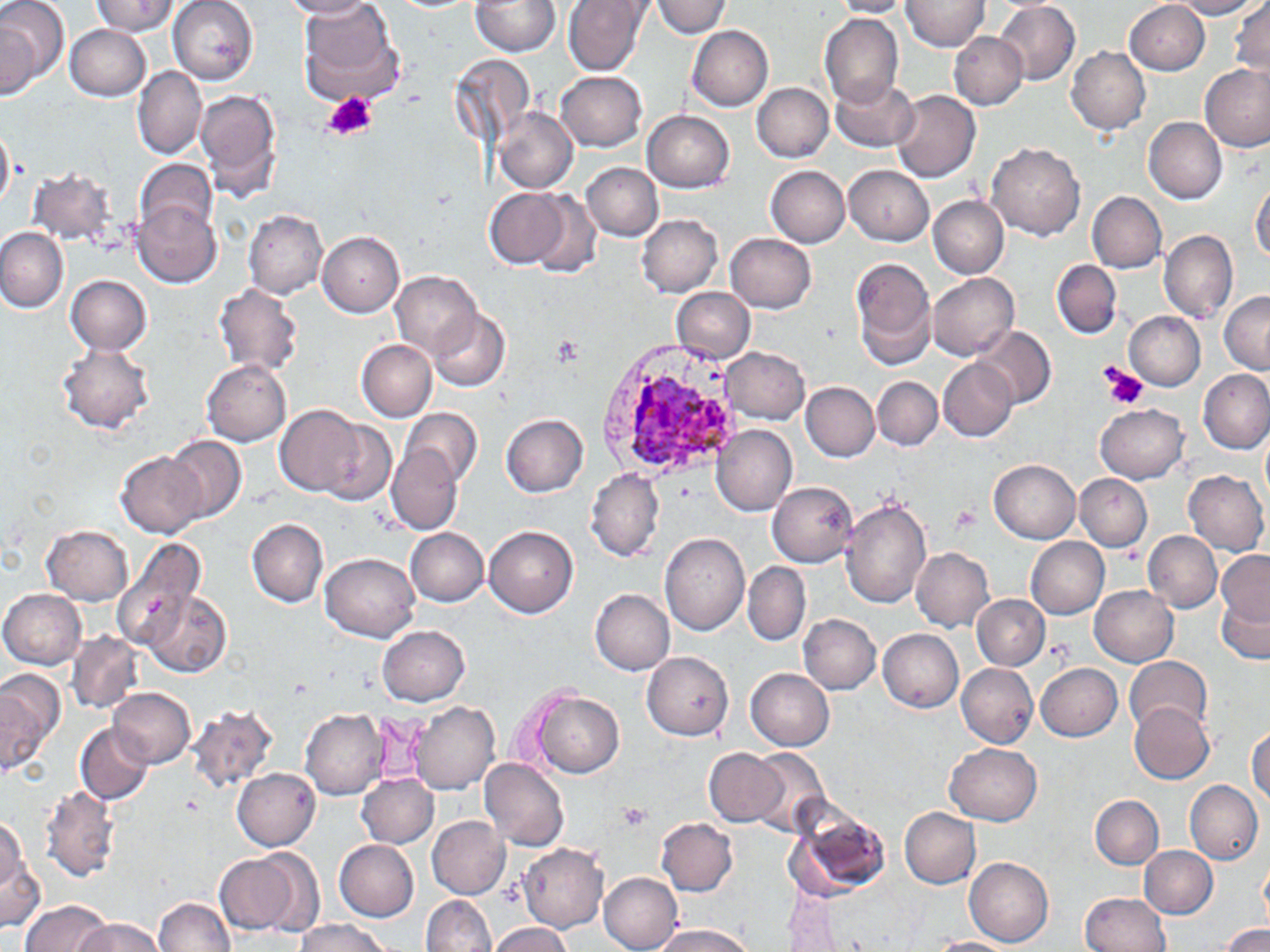
Approximate bounding boxes as (x1, y1, x2, y2) in pixels. Plasmodium vivax-infected red blood cell locations: (594, 337, 750, 482). Uninfected red blood cell locations: (0, 0, 67, 96), (169, 0, 258, 84), (282, 0, 378, 17), (471, 0, 560, 55), (562, 0, 650, 76), (651, 0, 733, 38), (1169, 0, 1266, 19), (91, 1, 180, 36), (299, 1, 408, 108), (832, 1, 912, 18), (901, 1, 991, 51), (1125, 1, 1210, 75), (996, 2, 1080, 85), (1231, 2, 1270, 79), (819, 13, 904, 106), (3, 16, 40, 100), (65, 25, 149, 100), (687, 26, 773, 111), (949, 32, 1026, 110), (1065, 48, 1150, 133), (1200, 64, 1269, 151), (132, 66, 206, 159), (558, 71, 646, 151), (830, 75, 918, 152), (752, 83, 833, 161), (196, 88, 282, 201), (889, 89, 979, 184), (495, 108, 576, 193), (643, 110, 735, 192), (1143, 116, 1226, 204), (0, 124, 15, 212), (986, 143, 1086, 241), (138, 159, 214, 237), (583, 162, 663, 241), (765, 166, 849, 247), (845, 166, 934, 246), (28, 167, 115, 248), (1250, 181, 1270, 264), (485, 188, 570, 266), (1087, 191, 1166, 272), (529, 192, 600, 277), (928, 197, 1008, 278), (134, 202, 221, 286), (243, 207, 327, 297), (637, 214, 722, 296), (0, 226, 69, 313), (1159, 230, 1237, 322), (318, 231, 404, 316), (726, 234, 816, 312), (851, 256, 938, 368), (1051, 259, 1121, 339), (393, 272, 481, 360), (927, 272, 1020, 360), (66, 275, 150, 354), (214, 283, 304, 377), (671, 287, 754, 363), (1218, 289, 1270, 373), (427, 309, 512, 391), (1125, 311, 1205, 390), (972, 327, 1055, 409), (357, 340, 436, 420), (58, 344, 154, 433), (721, 347, 810, 423), (939, 359, 1016, 441), (202, 360, 292, 446), (1199, 368, 1270, 453), (873, 376, 941, 449), (801, 382, 879, 461), (1094, 403, 1189, 483), (275, 406, 367, 496), (400, 408, 482, 489), (501, 413, 590, 496), (319, 417, 396, 506), (712, 426, 797, 515), (1260, 426, 1270, 506), (164, 436, 246, 523), (387, 443, 460, 533), (117, 452, 206, 537), (989, 459, 1082, 544), (586, 469, 664, 560), (1184, 469, 1268, 555), (1075, 474, 1152, 552), (768, 483, 858, 567), (840, 497, 933, 608), (247, 519, 329, 607), (43, 525, 134, 605), (484, 526, 578, 618), (407, 527, 489, 606), (1144, 530, 1222, 612), (660, 531, 749, 636), (111, 536, 206, 652), (1026, 537, 1109, 619), (912, 549, 994, 631), (1216, 551, 1270, 626), (320, 552, 421, 641), (742, 563, 811, 645), (1090, 585, 1178, 666), (0, 588, 86, 669), (590, 588, 675, 675), (145, 590, 231, 678), (964, 590, 1042, 740), (972, 594, 1051, 669), (1216, 595, 1269, 664), (798, 613, 880, 694), (377, 625, 470, 706), (878, 627, 964, 712), (67, 632, 144, 715), (642, 652, 734, 741), (1124, 656, 1213, 735), (957, 663, 1037, 747), (1037, 664, 1122, 741), (0, 668, 65, 769), (745, 668, 835, 750), (106, 685, 195, 769), (531, 691, 624, 777), (409, 700, 500, 795), (1129, 702, 1214, 783), (188, 704, 278, 792), (300, 710, 390, 798), (75, 722, 153, 805), (1246, 727, 1269, 805), (944, 742, 1041, 824), (705, 748, 789, 826), (746, 749, 833, 836), (480, 757, 568, 851), (233, 769, 320, 851), (358, 774, 437, 848), (1185, 780, 1262, 864), (40, 785, 120, 881), (1090, 795, 1163, 869), (781, 803, 892, 903), (900, 807, 981, 888), (426, 815, 510, 899), (656, 817, 738, 896), (0, 819, 40, 931), (334, 839, 419, 922), (519, 843, 609, 933), (1139, 845, 1217, 919), (214, 848, 317, 938), (963, 855, 1054, 946), (1259, 857, 1269, 927), (599, 872, 683, 952), (1079, 892, 1170, 951), (423, 895, 495, 950), (154, 897, 237, 952), (21, 900, 112, 952), (74, 918, 164, 952), (293, 920, 392, 952), (488, 923, 573, 952), (650, 923, 755, 951), (1219, 923, 1269, 952), (929, 937, 1018, 952). Platelet locations: (323, 91, 378, 140), (552, 337, 584, 369), (1099, 364, 1149, 411), (951, 506, 980, 536), (619, 801, 651, 827). Slide-level diagnosis: Plasmodium vivax. Single field of view. Light microscopy. Thin blood smear. 1000x magnification. May-Grünwald-Giemsa-stained preparation. Image is 1270×952 pixels.